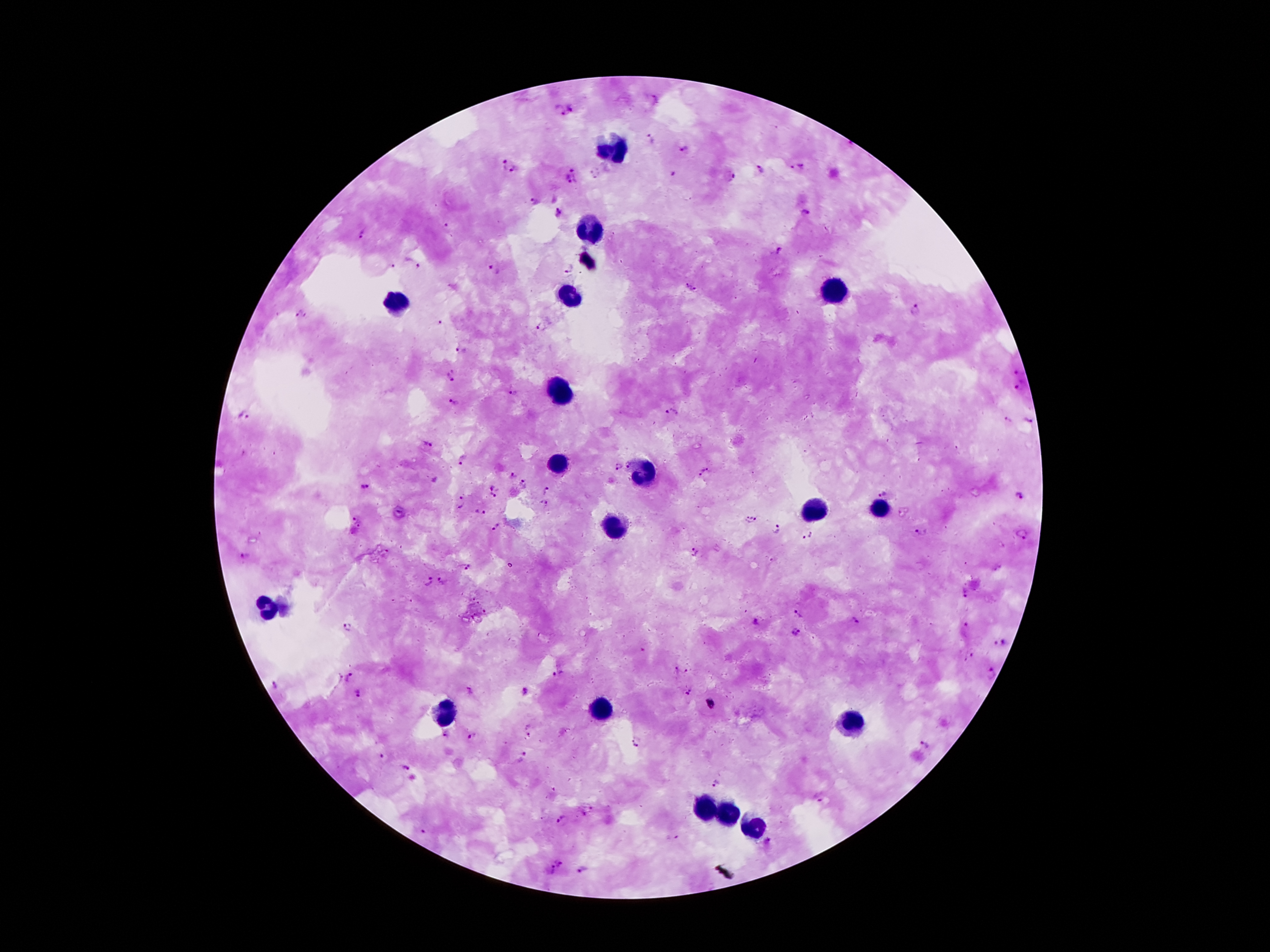 Giemsa-stained preparation. Patient malaria status: infected with Plasmodium falciparum. Single field of view. Image is 1270×952 pixels. Thick blood film. Photographed through the microscope eyepiece with a smartphone camera. 100x magnification.